Classify this cell by malaria status.
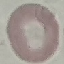
Uninfected.

stain: Giemsa
capture: smartphone through the microscope eyepiece
image_type: cell patch, automatically extracted from a larger field of view and resized to 64 × 64 pixels
preparation: thin blood film